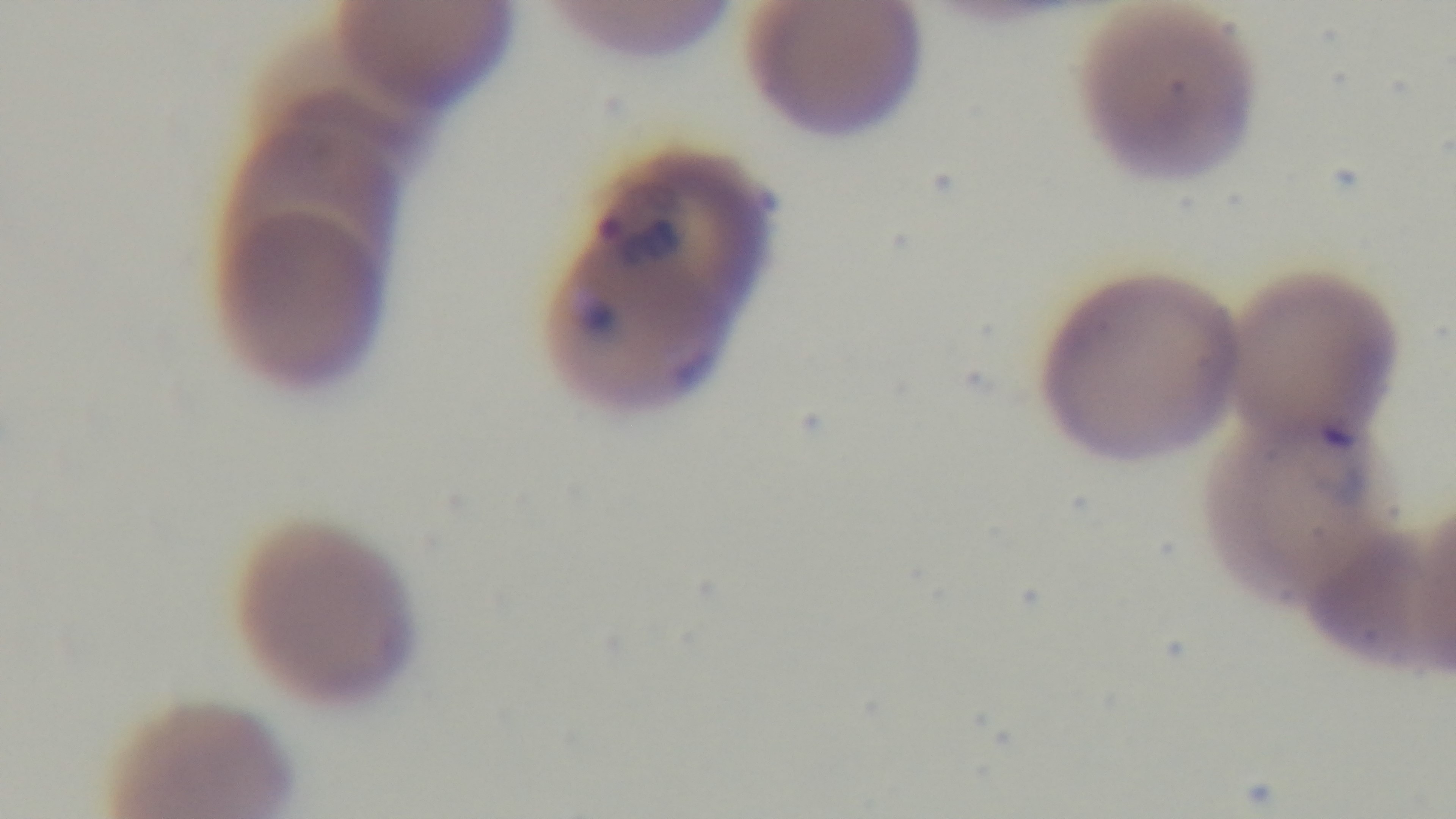
stain: Giemsa
modality: light microscopy
preparation: thin blood film
objective: 100x oil immersion
field_of_view: one from the slide
malaria_status: positive
capture: mounted 4K digital camera